Report the malaria status of this cell.
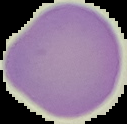

Uninfected.

The area outside the segmented cell region is set to black. Image is 127×124 pixels. From a thin blood smear.